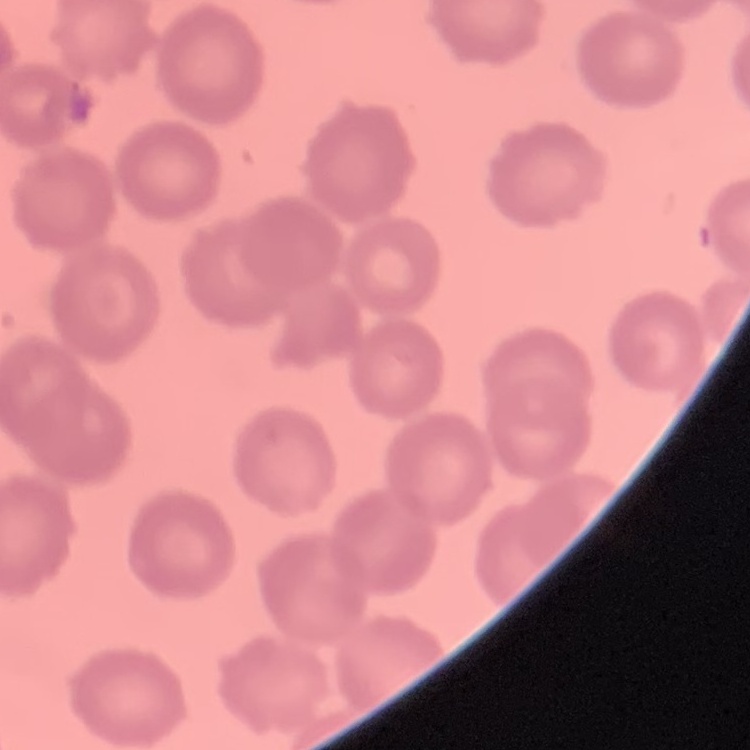 The red blood cells exhibit no rouleaux formation. Field's or Giemsa stain. One tile cut from a larger photomicrograph. Thin peripheral smear.